Classify this cell by malaria status.
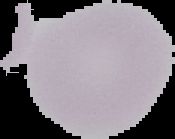
Uninfected.

preparation: thin blood smear
image_type: cell region segmented out of the field of view; surrounding area masked to black
image_size: 175×139 pixels